Give the extent of all Plasmodium ovale-infected red blood cells.
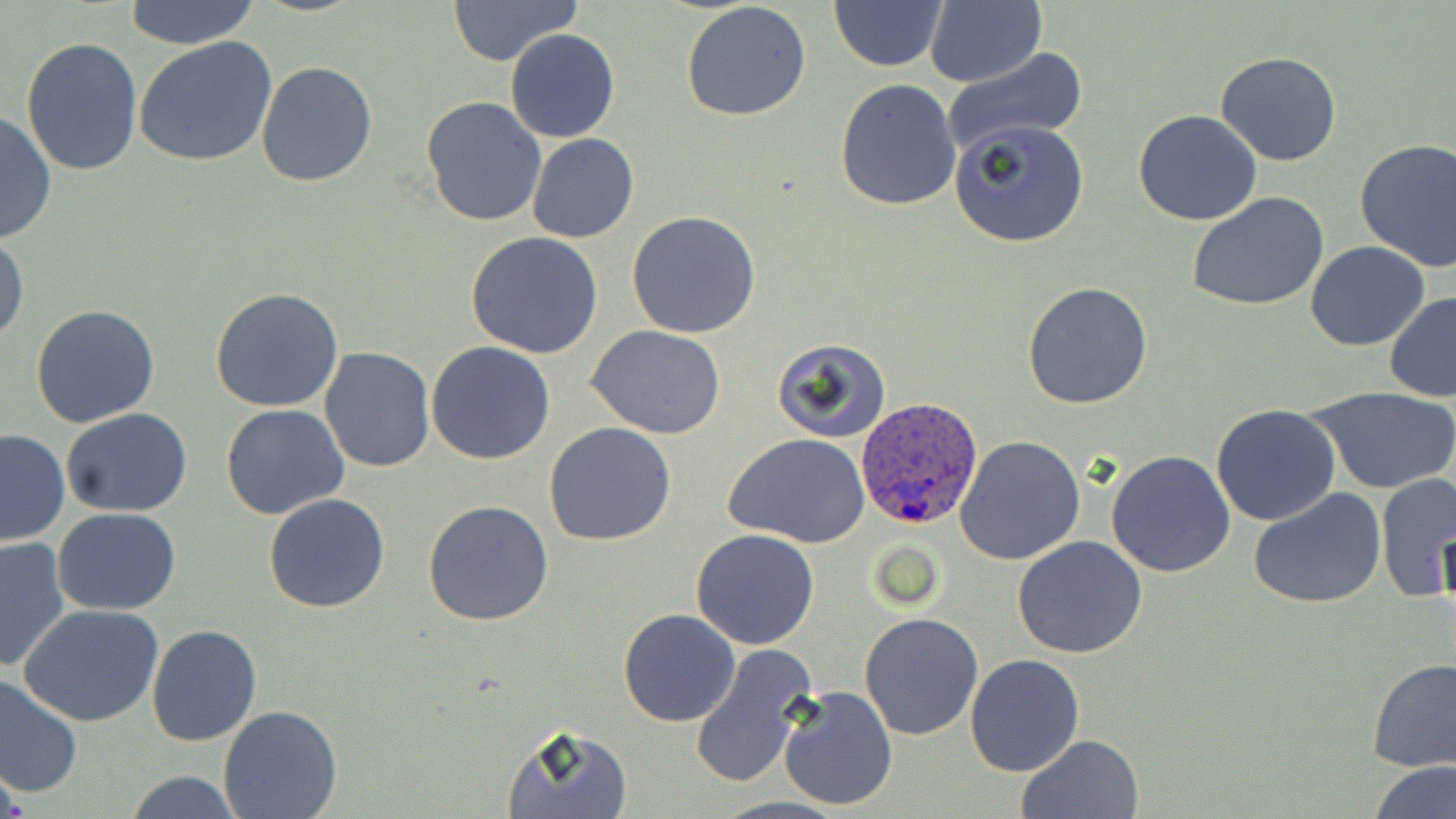

Approximate bounding boxes as named x1/y1/x2/y2 corners in pixels.
Plasmodium ovale-infected red blood cells: (x1=856, y1=397, x2=983, y2=530).

Summary:
  - Uninfected red blood cell locations: (x1=122, y1=0, x2=261, y2=50), (x1=445, y1=0, x2=585, y2=66), (x1=926, y1=0, x2=1046, y2=88), (x1=682, y1=1, x2=813, y2=122), (x1=830, y1=2, x2=945, y2=72), (x1=505, y1=28, x2=621, y2=143), (x1=21, y1=36, x2=143, y2=175), (x1=135, y1=38, x2=278, y2=169), (x1=941, y1=46, x2=1089, y2=158), (x1=1214, y1=52, x2=1344, y2=167), (x1=256, y1=61, x2=378, y2=187), (x1=833, y1=79, x2=963, y2=212), (x1=422, y1=95, x2=547, y2=227), (x1=0, y1=110, x2=56, y2=247), (x1=1132, y1=111, x2=1263, y2=226), (x1=949, y1=119, x2=1091, y2=248), (x1=526, y1=132, x2=639, y2=243), (x1=1354, y1=139, x2=1456, y2=271), (x1=1187, y1=193, x2=1330, y2=311), (x1=627, y1=211, x2=762, y2=338), (x1=464, y1=231, x2=604, y2=359), (x1=1, y1=232, x2=28, y2=347), (x1=1305, y1=240, x2=1431, y2=351), (x1=1022, y1=281, x2=1151, y2=410), (x1=210, y1=287, x2=345, y2=413), (x1=1384, y1=292, x2=1456, y2=402), (x1=31, y1=303, x2=161, y2=429), (x1=588, y1=326, x2=728, y2=440), (x1=769, y1=336, x2=893, y2=443), (x1=425, y1=340, x2=556, y2=464), (x1=317, y1=347, x2=436, y2=472), (x1=1306, y1=384, x2=1456, y2=496), (x1=221, y1=403, x2=350, y2=519), (x1=1210, y1=404, x2=1341, y2=526), (x1=62, y1=408, x2=192, y2=519), (x1=544, y1=422, x2=676, y2=546), (x1=0, y1=430, x2=71, y2=547), (x1=725, y1=434, x2=870, y2=548), (x1=954, y1=435, x2=1086, y2=566), (x1=1106, y1=450, x2=1236, y2=577), (x1=1376, y1=472, x2=1455, y2=602), (x1=1249, y1=488, x2=1387, y2=609), (x1=263, y1=491, x2=391, y2=613), (x1=423, y1=499, x2=553, y2=626), (x1=53, y1=508, x2=182, y2=616), (x1=691, y1=528, x2=820, y2=649), (x1=1012, y1=535, x2=1147, y2=660), (x1=0, y1=537, x2=70, y2=674), (x1=19, y1=603, x2=164, y2=727), (x1=618, y1=609, x2=740, y2=727), (x1=859, y1=612, x2=983, y2=741), (x1=146, y1=625, x2=262, y2=747), (x1=688, y1=644, x2=818, y2=789), (x1=965, y1=653, x2=1085, y2=775), (x1=1366, y1=657, x2=1455, y2=771), (x1=0, y1=673, x2=84, y2=800), (x1=775, y1=682, x2=898, y2=810), (x1=219, y1=703, x2=343, y2=819), (x1=501, y1=723, x2=634, y2=819), (x1=1017, y1=734, x2=1144, y2=819), (x1=1369, y1=759, x2=1455, y2=819), (x1=124, y1=771, x2=244, y2=818)
  - Slide-level diagnosis: Plasmodium ovale
  - Image size: 1456×819 pixels
  - Modality: optical microscopy
  - Magnification: 1000x
  - Preparation: thin blood film
  - Field of view: single
  - Stain: May-Grünwald-Giemsa